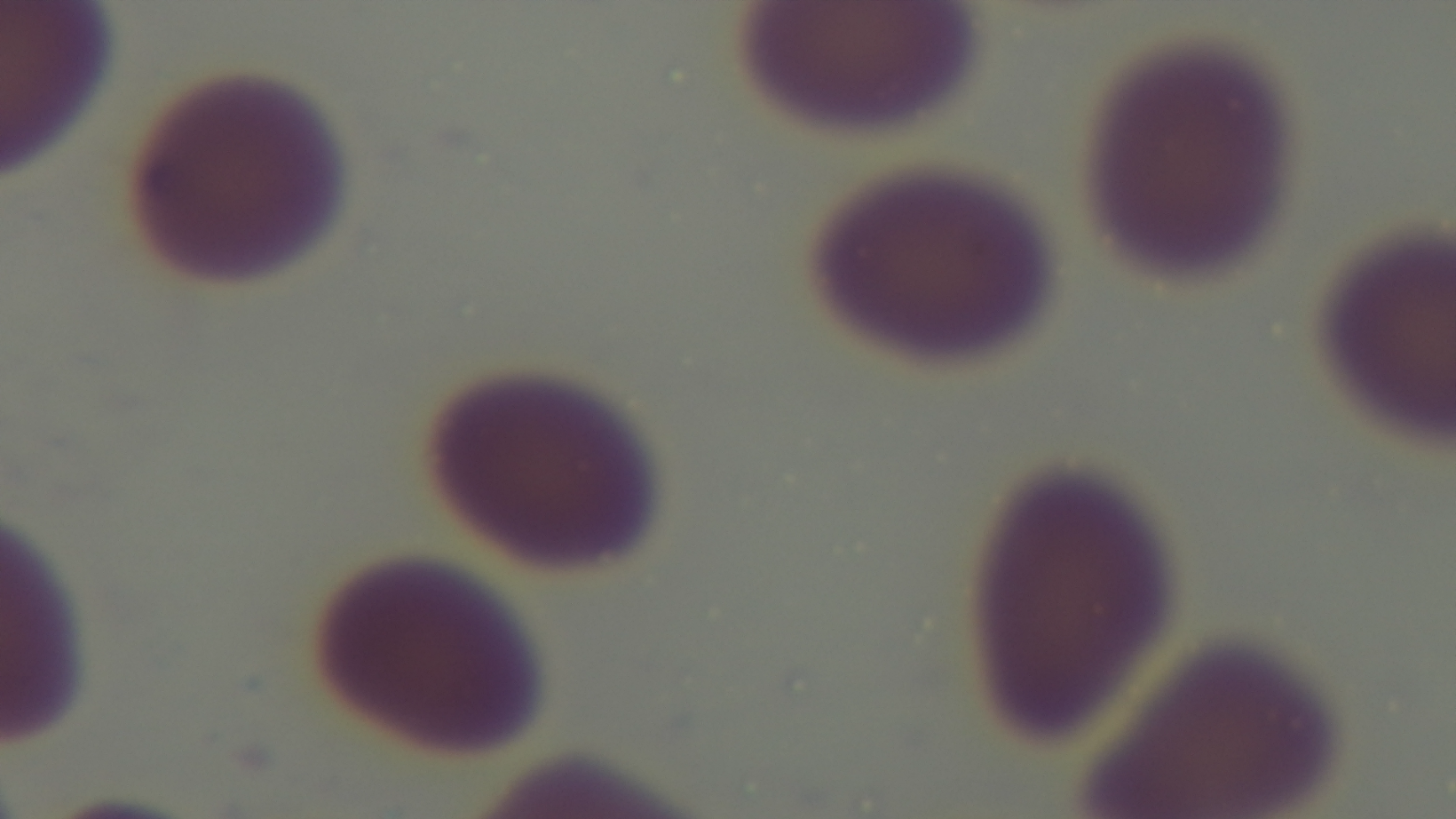
Photomicrograph. Malaria status: uninfected. Giemsa-stained. One field from the slide. 100x oil-immersion objective. Captured with a mounted 4K digital camera. Preparation: thin smear.